Assess this cell for malaria.
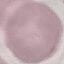

It is uninfected.

Summary:
  - Preparation: thin blood film
  - Capture: smartphone through the microscope eyepiece
  - Image type: cell patch, automatically extracted from a larger field of view and resized to 64 × 64 pixels
  - Stain: Giemsa